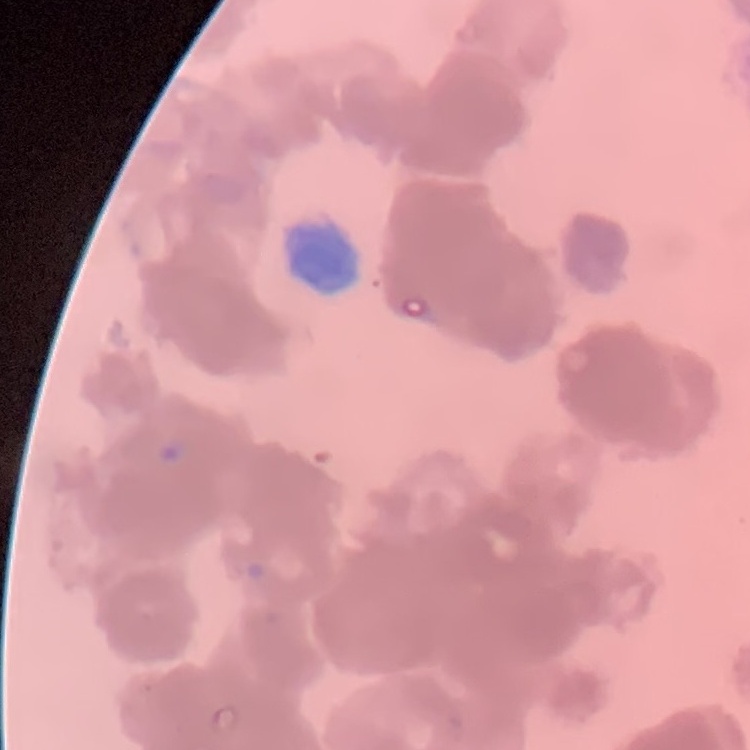

red blood cell morphology = rouleaux formation
stain = Field's or Giemsa
preparation = thin peripheral smear
image type = one tile cut from a larger photomicrograph